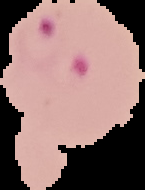

{
  "image_size": "145×190 pixels",
  "result": "malaria parasites detected",
  "preparation": "thin blood smear",
  "image_type": "segmented cell region on a black background"
}